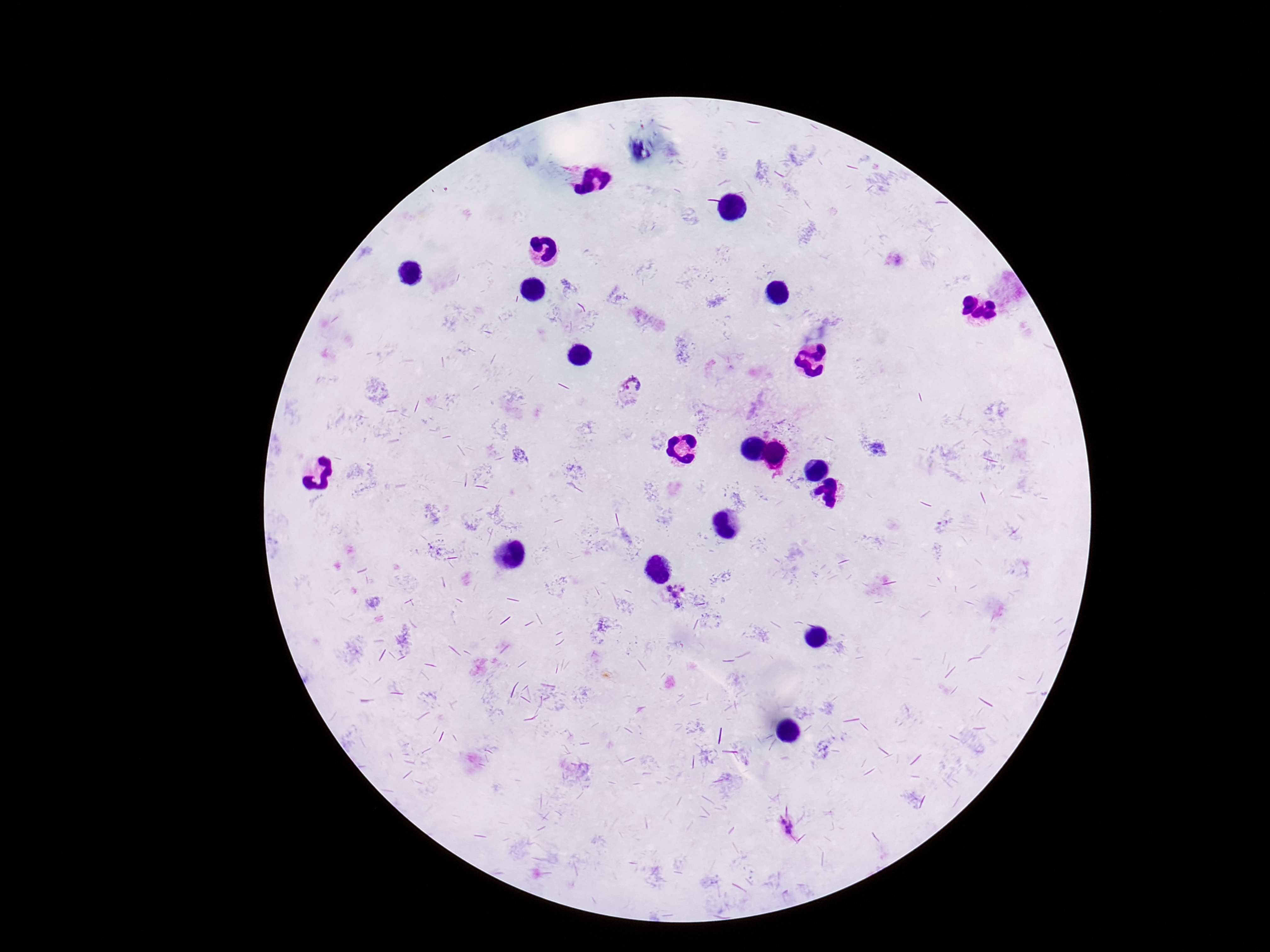 Approximate centers as (x, y) in pixels. Plasmodium parasite locations: (632, 391), (675, 590), (787, 829). Thick blood smear. 100x magnification. Image is 1270×952 pixels. Single field of view. Photographed through the microscope eyepiece with a smartphone camera. Patient malaria status: positive. Giemsa stain.